State which parasite is depicted.
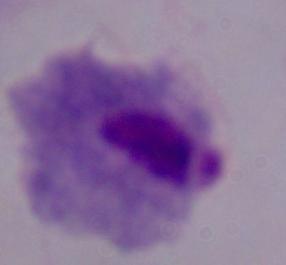
A trichomonad.

Micrograph. 1000x magnification.